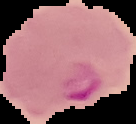
image type = cell region segmented out of the field of view; surrounding area masked to black
image size = 136×124 pixels
preparation = thin blood smear
result = Plasmodium parasites identified